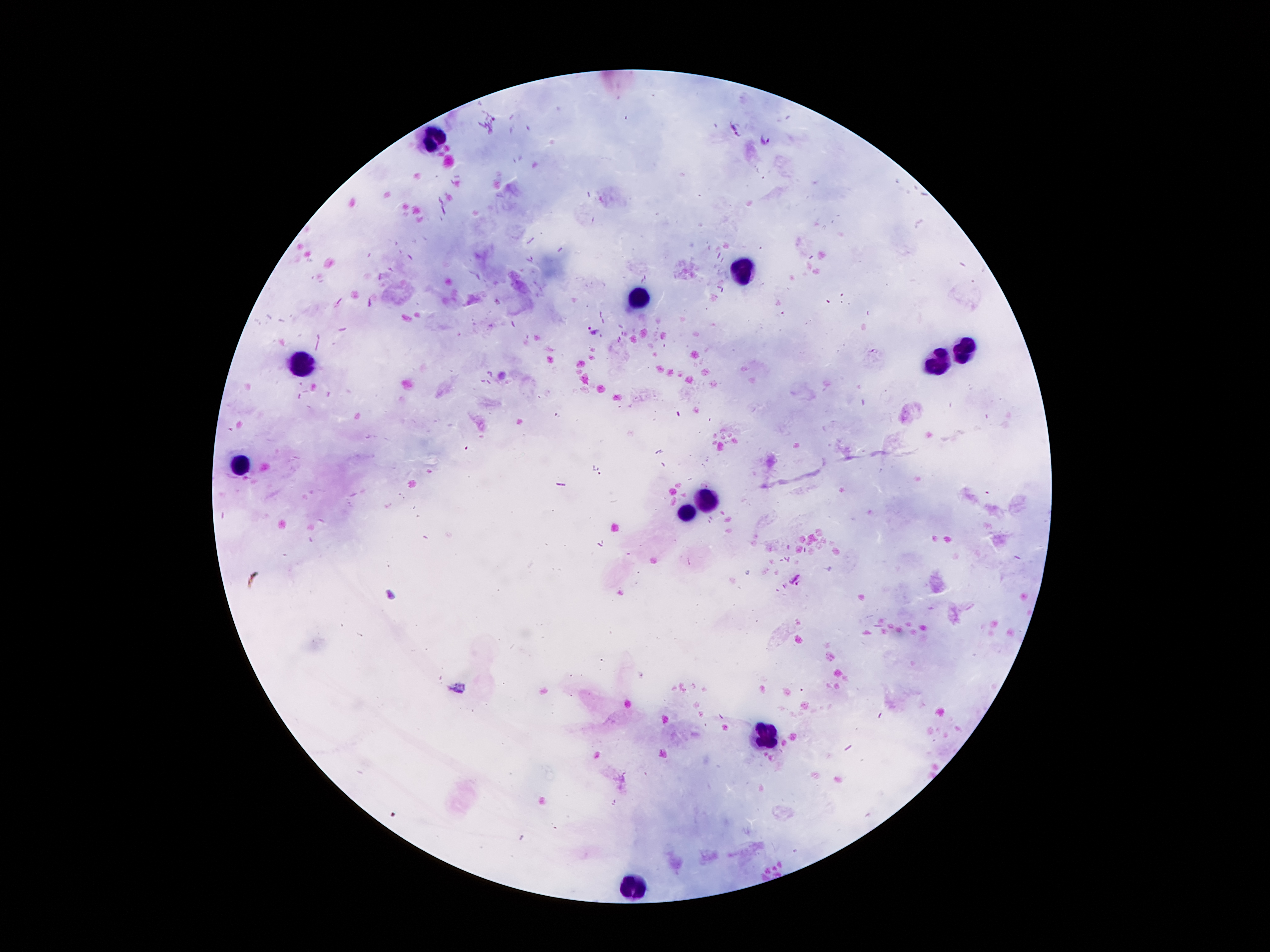

{
  "patient_malaria_status": "infected with Plasmodium falciparum",
  "plasmodium_parasite_locations": "approximate centers as (x, y) in pixels: (734, 128), (765, 138), (595, 330), (796, 579)",
  "image_size": "1270×952 pixels",
  "leukocyte_locations": "approximate centers as (x, y) in pixels: (429, 139), (747, 273), (640, 300), (963, 357), (940, 364), (304, 368), (243, 464), (706, 502), (686, 514), (765, 734), (629, 886)",
  "preparation": "thick blood smear",
  "field_of_view": "one from this slide",
  "stain": "Giemsa",
  "magnification": "100x",
  "capture": "smartphone through the microscope eyepiece"
}